Report the malaria status of this cell.
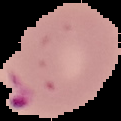

Parasitized.

The area outside the segmented cell region is set to black. From a thin blood smear. Image is 121×121 pixels.